Give the preparation type.
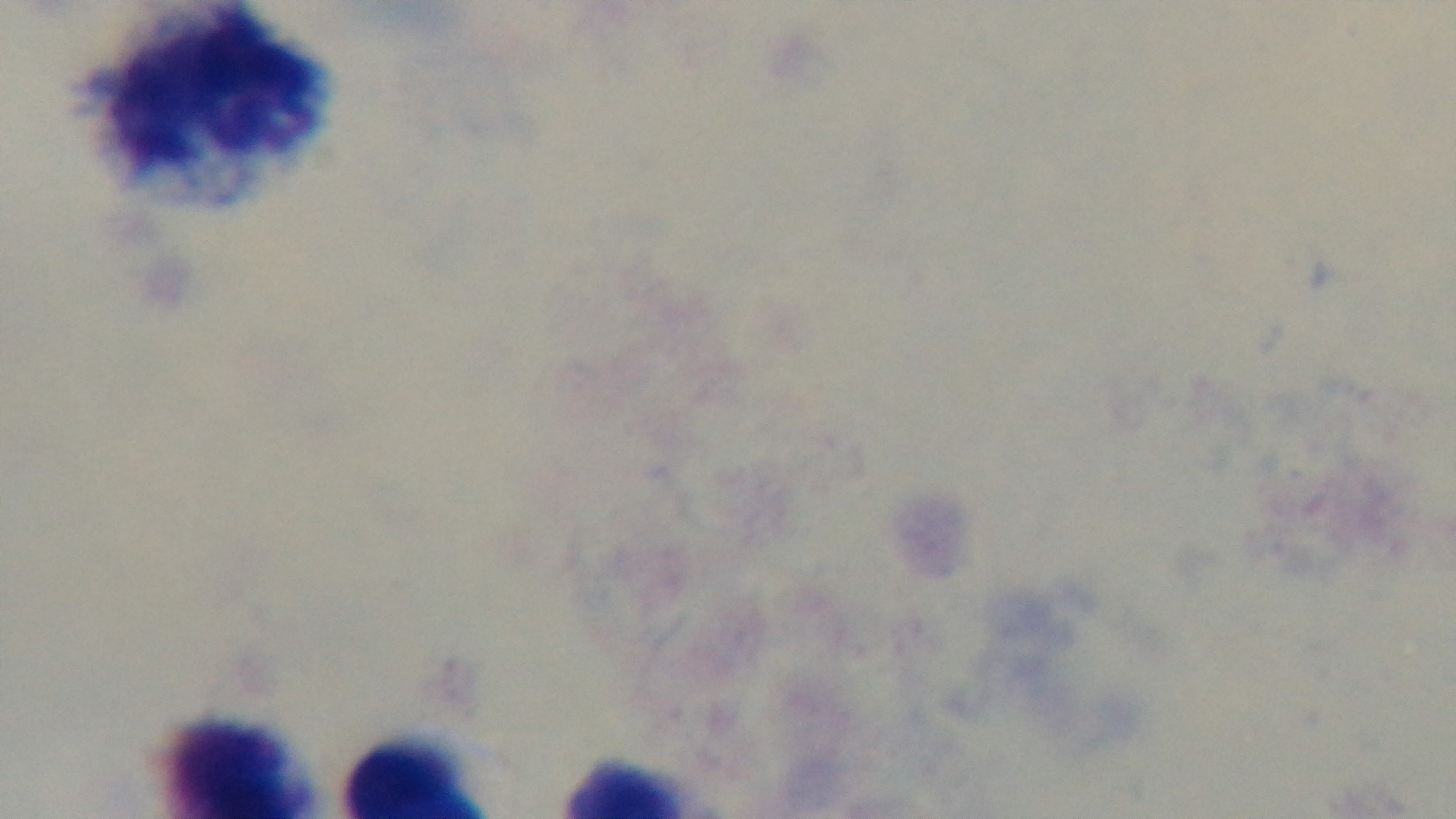

A thick smear.

Single field of view. Captured with a mounted 4K digital camera. Malaria status: uninfected. Giemsa-stained. Oil-immersion objective, 100x. Light microscopy.